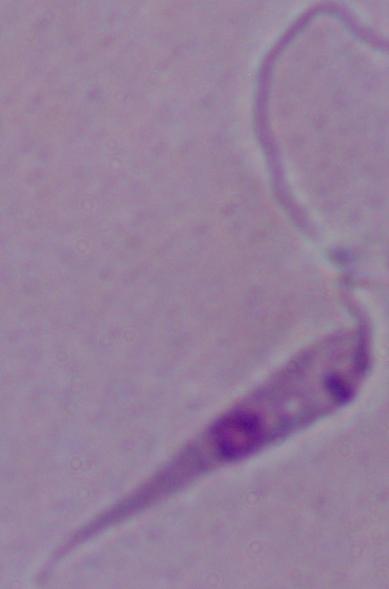 Micrograph. A Leishmania parasite is seen. Captured at 1000x magnification.